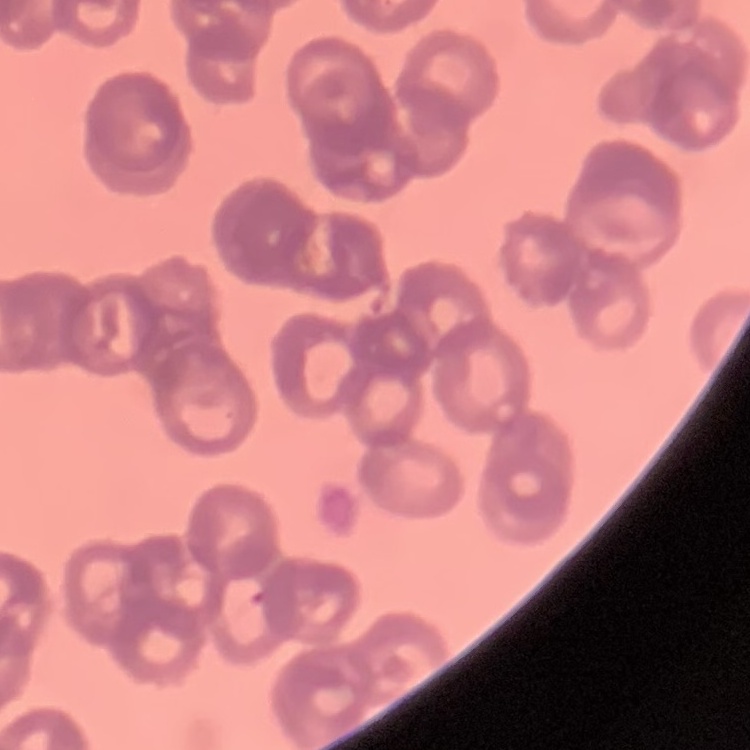

The red blood cells show rouleaux formation. Stained with either Field's or Giemsa. One tile cut from a larger photomicrograph. Thin peripheral smear.